Locate every uninfected red blood cell.
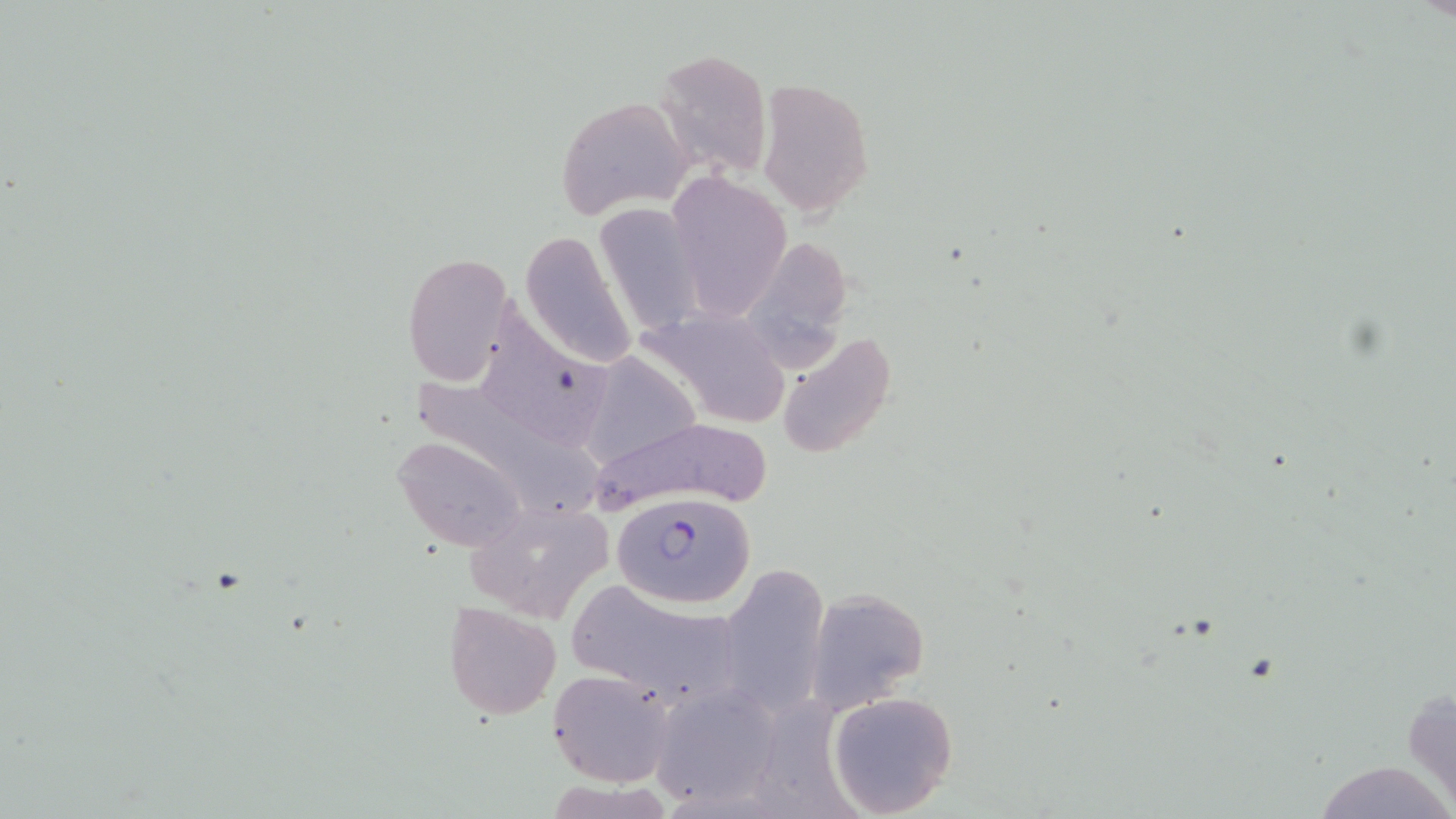
Approximate bounding boxes as (x1, y1, x2, y2) in pixels.
Uninfected red blood cells: (652, 47, 774, 177), (757, 77, 874, 218), (557, 95, 694, 219), (662, 173, 790, 320), (597, 203, 702, 335), (520, 231, 637, 368), (747, 245, 863, 382), (402, 251, 517, 386), (488, 301, 613, 445), (642, 306, 793, 428), (775, 333, 898, 463), (585, 353, 700, 465), (405, 369, 606, 523), (591, 413, 775, 512), (394, 435, 527, 551), (465, 499, 612, 623), (720, 564, 830, 721), (568, 578, 745, 707), (804, 589, 928, 712), (444, 600, 562, 718), (547, 669, 674, 787), (649, 685, 779, 809), (826, 691, 959, 817), (1309, 760, 1453, 819).

{
  "plasmodium_falciparum_infected_red_blood_cell_locations": "approximate bounding boxes as (x1, y1, x2, y2) in pixels: (614, 494, 751, 605)",
  "slide_level_diagnosis": "Plasmodium falciparum",
  "stain": "May-Grünwald-Giemsa",
  "magnification": "1000x",
  "preparation": "thin blood film",
  "modality": "optical microscopy",
  "image_size": "1456×819 pixels",
  "field_of_view": "one of a larger specimen"
}